Give the preparation type.
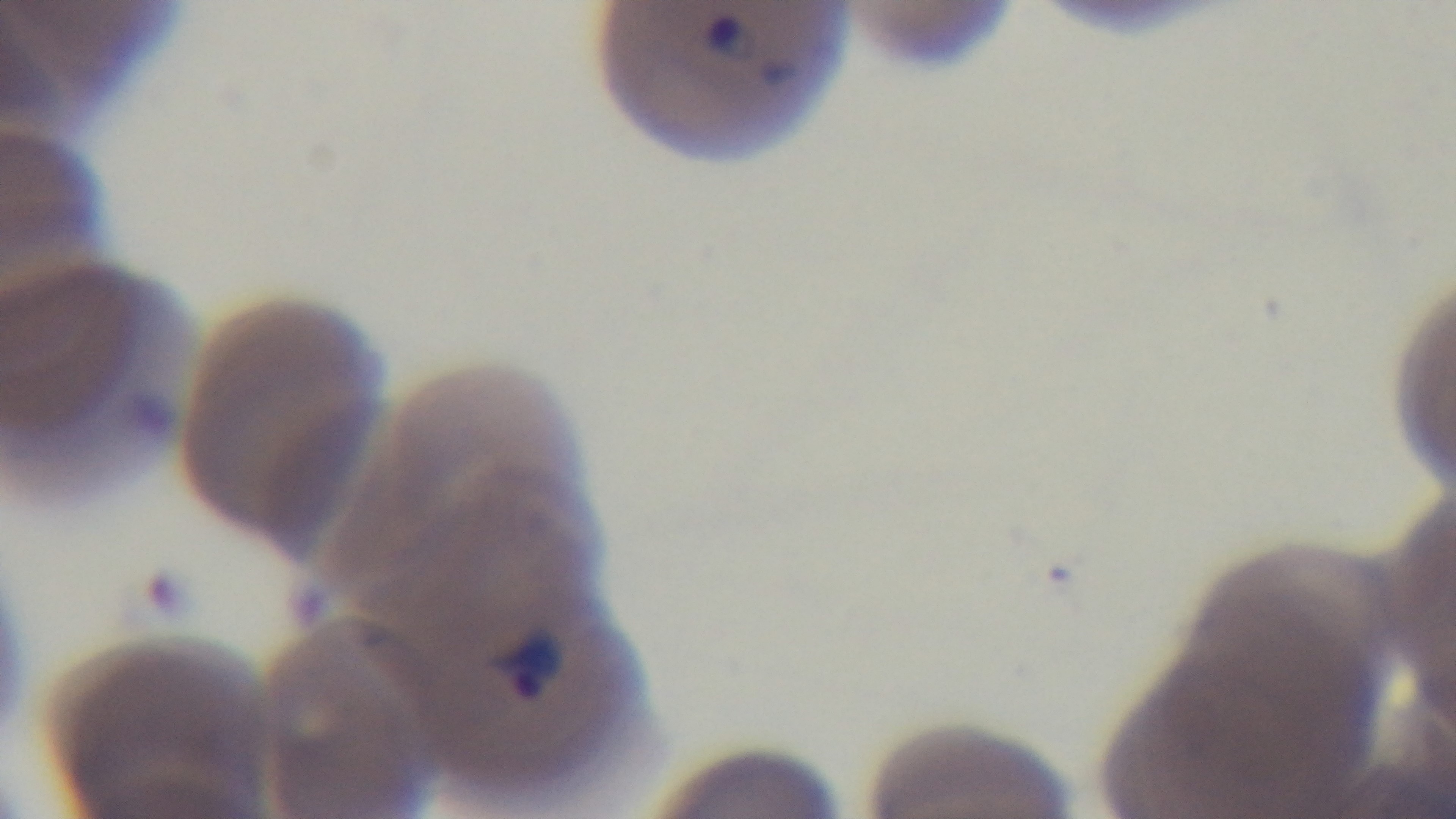

It is a thin blood film.

One field from the slide. Photomicrograph. Mounted 4K digital camera. 100x oil-immersion objective. Malaria status: positive. Giemsa stain.